State the blood parasite species.
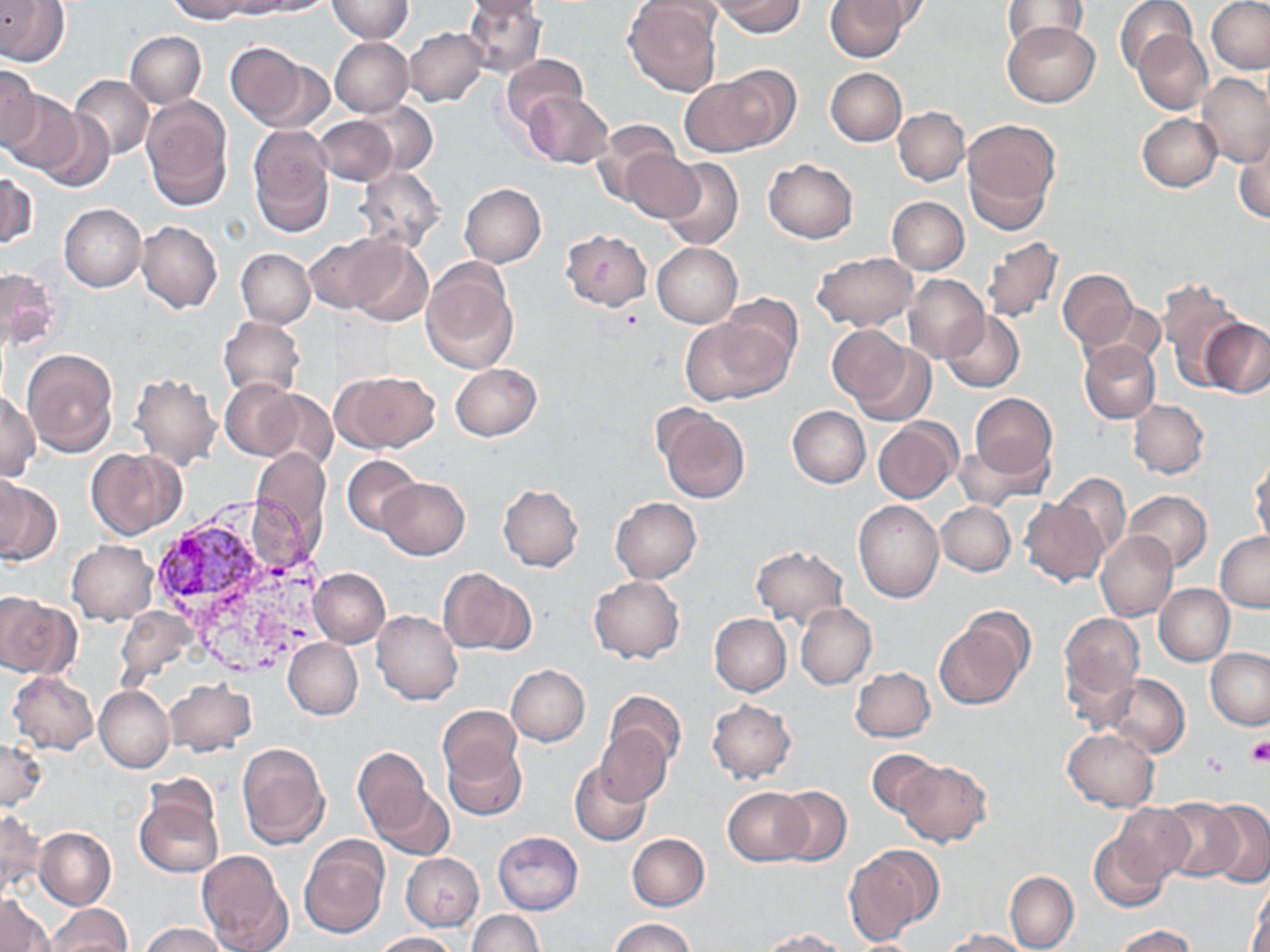

Plasmodium vivax.

Approximate bounding boxes as [x1, y1, x2, y2] in pixels. Plasmodium vivax-infected red blood cell locations: [157, 523, 267, 608]. Uninfected red blood cell locations: [0, 0, 70, 66], [163, 0, 255, 23], [247, 0, 335, 16], [325, 0, 413, 43], [462, 0, 546, 79], [465, 0, 544, 22], [716, 0, 804, 37], [824, 0, 911, 62], [846, 0, 933, 39], [1002, 0, 1088, 52], [1115, 0, 1195, 75], [623, 1, 723, 96], [1207, 1, 1270, 73], [1004, 20, 1099, 107], [403, 27, 487, 107], [124, 30, 206, 107], [1132, 32, 1212, 114], [329, 37, 413, 117], [225, 42, 323, 131], [500, 54, 588, 132], [0, 66, 39, 146], [826, 68, 906, 146], [1198, 72, 1270, 168], [71, 75, 153, 157], [75, 75, 219, 178], [679, 76, 781, 157], [0, 90, 84, 175], [523, 92, 614, 168], [139, 96, 232, 208], [355, 100, 437, 177], [37, 107, 116, 193], [893, 108, 969, 185], [1137, 113, 1222, 192], [311, 115, 399, 187], [593, 119, 682, 203], [962, 119, 1060, 229], [248, 126, 334, 236], [1234, 131, 1270, 225], [622, 148, 704, 223], [657, 157, 744, 251], [764, 159, 858, 243], [355, 167, 444, 251], [0, 170, 37, 248], [459, 184, 546, 267], [887, 196, 968, 275], [59, 204, 146, 291], [136, 220, 222, 313], [561, 229, 652, 311], [304, 235, 404, 314], [980, 237, 1062, 325], [346, 241, 433, 327], [652, 242, 742, 327], [235, 249, 315, 329], [812, 251, 918, 332], [420, 256, 518, 376], [1, 267, 59, 352], [1059, 269, 1136, 349], [902, 274, 989, 364], [1155, 277, 1242, 388], [721, 294, 802, 375], [1084, 300, 1165, 372], [942, 311, 1025, 392], [681, 312, 794, 406], [217, 316, 304, 402], [1201, 319, 1270, 397], [831, 328, 930, 422], [1080, 341, 1160, 424], [22, 349, 118, 456], [451, 363, 541, 441], [335, 371, 440, 453], [130, 372, 223, 472], [221, 380, 302, 459], [252, 389, 337, 470], [0, 391, 40, 480], [969, 393, 1056, 478], [1128, 400, 1209, 478], [655, 406, 750, 504], [788, 406, 869, 488], [873, 417, 961, 503], [953, 439, 1049, 511], [87, 447, 185, 540], [251, 448, 330, 549], [342, 454, 423, 537], [1249, 455, 1269, 549], [1051, 472, 1131, 558], [0, 474, 28, 558], [0, 477, 60, 567], [379, 477, 469, 560], [499, 484, 583, 572], [1123, 490, 1213, 572], [611, 497, 701, 583], [1021, 498, 1107, 586], [854, 500, 944, 602], [935, 502, 1015, 575], [1095, 531, 1178, 622], [1215, 532, 1270, 611], [68, 540, 158, 624], [751, 545, 848, 627], [298, 566, 377, 709], [309, 567, 390, 648], [439, 568, 533, 656], [589, 575, 683, 663], [1155, 583, 1233, 665], [0, 594, 80, 678], [795, 603, 877, 688], [372, 610, 462, 704], [933, 612, 1031, 711], [709, 613, 790, 696], [1059, 613, 1144, 704], [283, 638, 362, 720], [1206, 648, 1270, 730], [1060, 654, 1141, 735], [505, 664, 590, 745], [850, 667, 935, 742], [8, 670, 98, 754], [1106, 675, 1190, 758], [164, 679, 256, 756], [94, 685, 174, 772], [604, 690, 687, 771], [707, 699, 796, 784], [437, 706, 522, 790], [596, 726, 672, 805], [1062, 728, 1159, 811], [0, 738, 45, 810], [444, 739, 527, 820], [236, 743, 330, 850], [353, 747, 432, 840], [867, 748, 945, 818], [896, 759, 991, 847], [569, 761, 652, 847], [368, 780, 454, 860], [773, 786, 851, 864], [723, 787, 812, 864], [134, 789, 223, 879], [1158, 799, 1242, 880], [1203, 801, 1270, 887], [1112, 803, 1199, 885], [0, 809, 44, 899], [1089, 824, 1182, 913], [34, 828, 116, 909], [493, 831, 582, 913], [627, 833, 709, 911], [299, 838, 389, 939], [846, 846, 941, 939], [196, 850, 292, 952], [401, 853, 483, 931], [1005, 871, 1079, 952], [1248, 878, 1270, 952], [1, 894, 53, 952], [48, 904, 129, 952], [469, 910, 543, 952], [610, 918, 694, 952], [142, 922, 226, 952], [1114, 925, 1197, 952], [760, 928, 847, 952], [944, 929, 1028, 951], [374, 931, 457, 952]. Platelet locations: [1245, 737, 1270, 766], [1203, 752, 1231, 780]. Image is 1270×952 pixels. May-Grünwald-Giemsa stain. One field of a larger specimen. Light microscopy. 1000x magnification. Thin blood smear.